Classify this cell by malaria status.
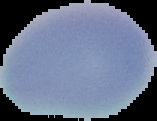
It is uninfected.

Summary:
  - Image size: 157×121 pixels
  - Preparation: thin blood film
  - Image type: segmented cell region on a black background